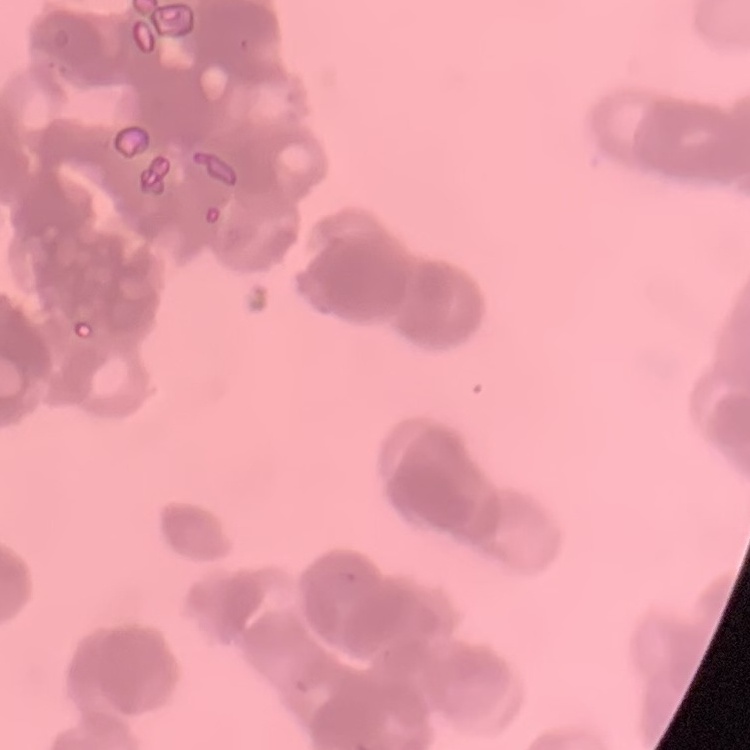
Summary:
  - Erythrocyte morphology: rouleaux formation
  - Image type: square crop of a larger photomicrograph
  - Preparation: thin peripheral smear
  - Stain: Field's or Giemsa